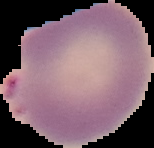
Cell region segmented out of the field of view; the surrounding area is masked to black. Result: malaria parasites identified. Image is 154×148 pixels. From a thin blood smear.